State which parasite is depicted.
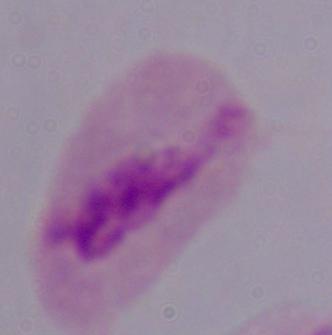

This is a trichomonad.

magnification: 1000x
modality: micrograph